Assess this cell for malaria.
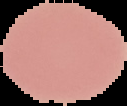

Uninfected.

Summary:
  - Preparation: thin blood film
  - Image type: segmented cell region on a black background
  - Image size: 127×106 pixels